Locate every blood parasite and identify its species.
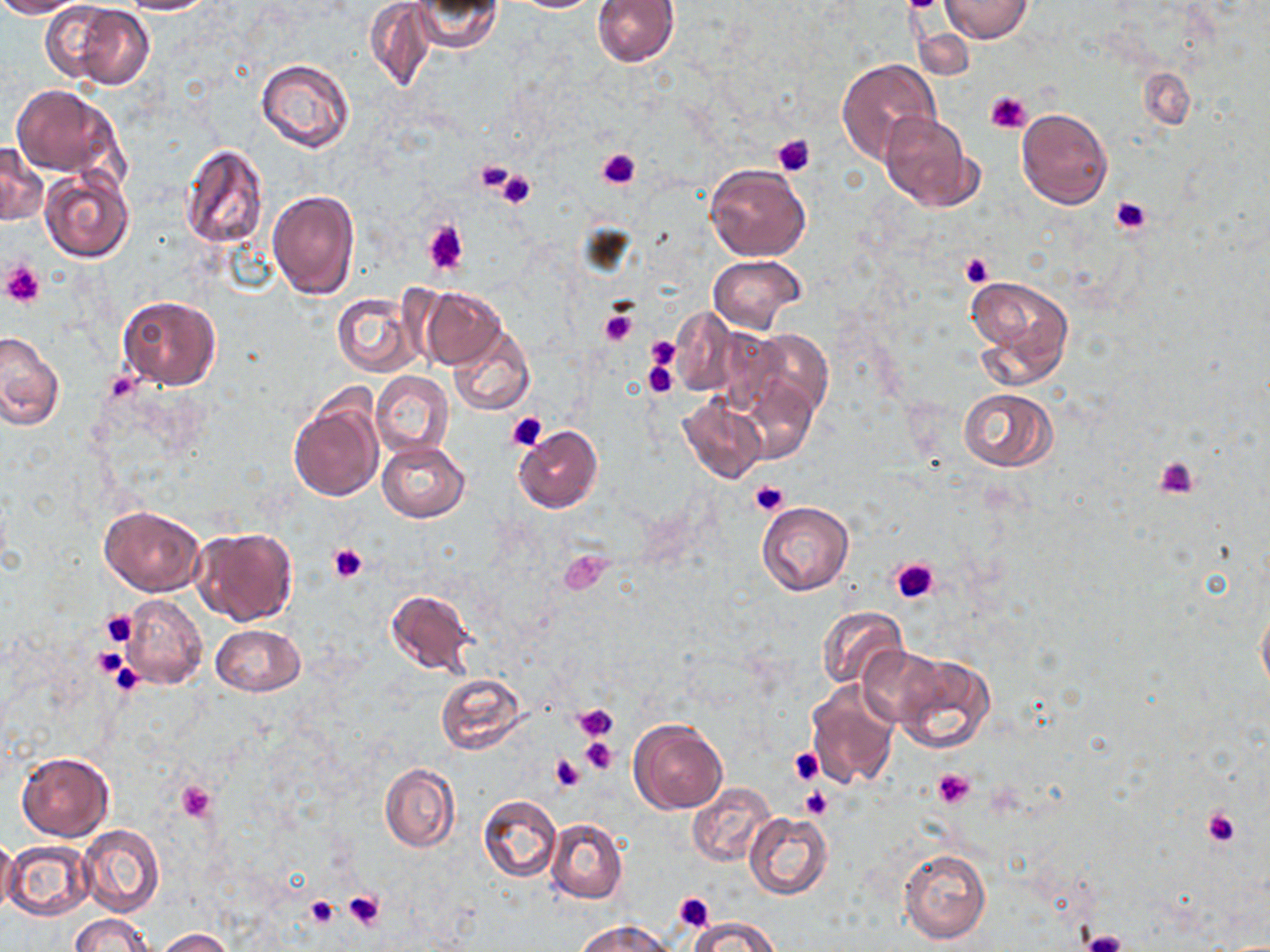
No blood parasites observed.

Approximate bounding boxes as (x1, y1, x2, y2) in pixels. Platelet locations: (900, 0, 942, 12), (984, 90, 1032, 134), (772, 134, 816, 177), (597, 148, 640, 190), (471, 158, 517, 195), (497, 167, 538, 209), (1110, 196, 1153, 235), (423, 221, 469, 275), (960, 252, 992, 288), (2, 260, 46, 307), (598, 309, 637, 347), (646, 337, 680, 369), (642, 361, 679, 398), (506, 411, 549, 452), (1154, 457, 1200, 500), (749, 480, 789, 517), (327, 544, 368, 583), (560, 549, 614, 595), (891, 558, 939, 602), (100, 610, 137, 647), (92, 646, 128, 681), (102, 656, 149, 694), (574, 704, 618, 741), (581, 737, 617, 776), (787, 747, 824, 785), (551, 754, 585, 792), (933, 769, 975, 810), (177, 782, 217, 822), (801, 788, 832, 819), (1202, 805, 1242, 849), (342, 889, 385, 931), (673, 891, 715, 929), (305, 895, 339, 928), (1080, 930, 1129, 952). Uninfected red blood cell locations: (0, 0, 89, 17), (117, 0, 218, 15), (408, 0, 503, 52), (511, 0, 600, 12), (591, 0, 678, 66), (940, 0, 1033, 42), (40, 1, 155, 88), (364, 1, 437, 90), (837, 58, 941, 163), (255, 59, 355, 153), (1139, 68, 1194, 129), (12, 83, 121, 179), (1016, 108, 1112, 208), (878, 112, 975, 211), (0, 142, 47, 226), (178, 143, 270, 249), (704, 163, 811, 261), (39, 168, 135, 263), (266, 189, 360, 300), (708, 254, 806, 333), (963, 274, 1075, 389), (417, 286, 507, 371), (333, 292, 420, 377), (117, 296, 220, 390), (669, 307, 744, 398), (447, 324, 533, 415), (705, 326, 790, 418), (746, 327, 833, 420), (0, 332, 64, 433), (371, 371, 453, 458), (737, 375, 818, 465), (959, 388, 1059, 471), (288, 390, 385, 502), (675, 396, 767, 484), (513, 425, 604, 514), (377, 440, 470, 522), (757, 501, 853, 595), (99, 505, 204, 596), (191, 526, 299, 626), (384, 589, 477, 675), (120, 594, 208, 690), (1256, 601, 1270, 699), (817, 605, 908, 691), (212, 624, 304, 696), (859, 646, 948, 727), (896, 654, 996, 753), (434, 672, 528, 754), (804, 679, 900, 790), (628, 718, 727, 815), (16, 750, 114, 842), (381, 763, 459, 852), (688, 784, 775, 866), (478, 795, 562, 882), (744, 812, 833, 899), (546, 819, 627, 903), (77, 823, 164, 917), (0, 837, 19, 914), (3, 841, 95, 921), (899, 848, 991, 944), (70, 914, 153, 952), (686, 915, 780, 951), (577, 920, 677, 952), (155, 928, 234, 951). Slide-level diagnosis: negative for blood parasites. May-Grünwald-Giemsa stain. Image is 1270×952 pixels. Single field of view. Thin blood film. Light microscopy. Captured at 1000x magnification.